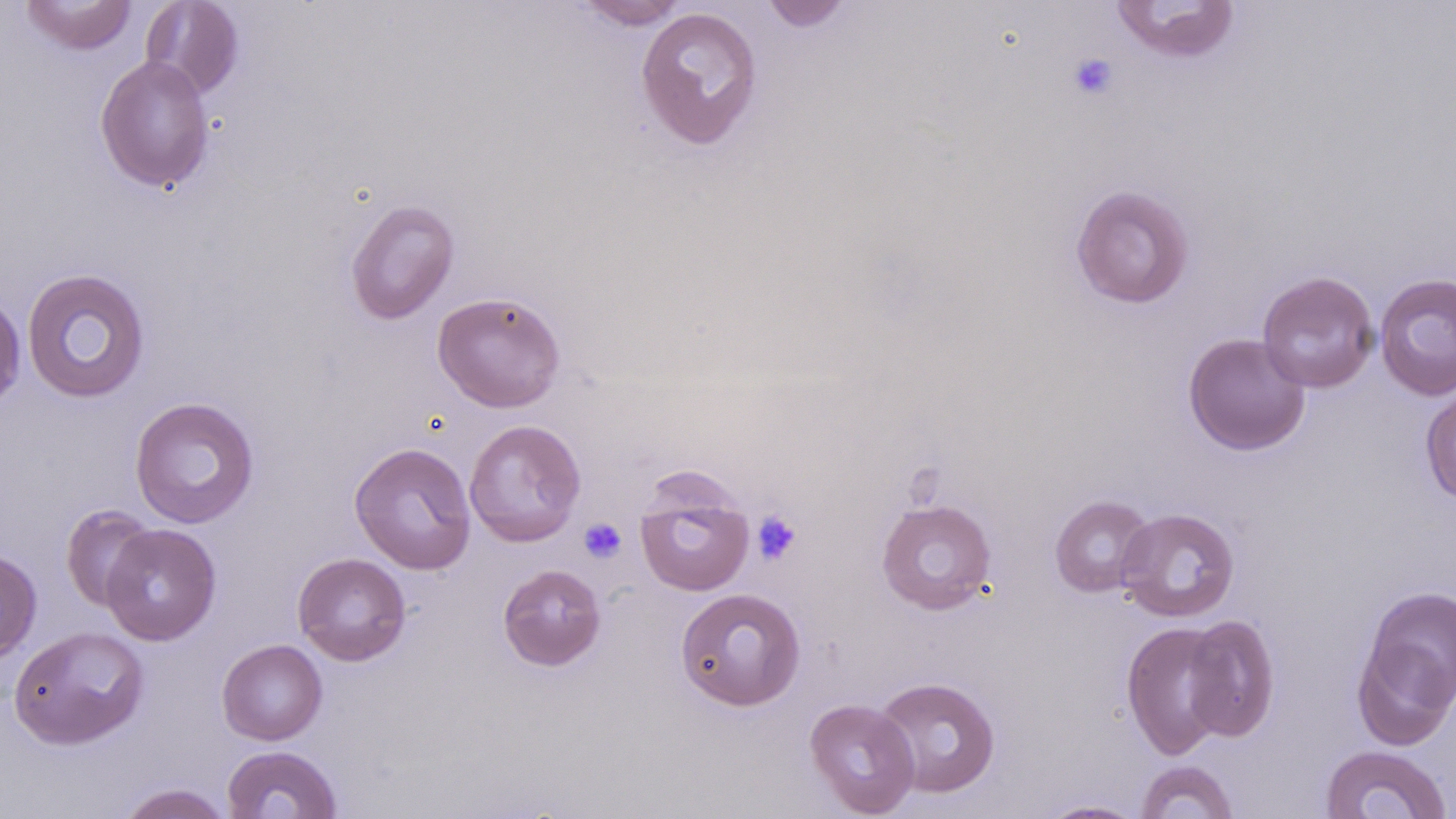
Summary:
  - Coordinate format: approximate bounding boxes as (x1,y1)-(x2,y2) corner pairs in pixels
  - Uninfected red blood cell locations: (21,0)-(137,55), (140,0)-(244,100), (1110,0)-(1241,62), (573,1)-(690,29), (759,1)-(855,32), (635,6)-(764,150), (95,55)-(215,193), (1070,184)-(1195,310), (345,197)-(460,325), (21,267)-(150,404), (1257,270)-(1380,394), (1374,273)-(1456,401), (432,291)-(566,413), (0,293)-(26,413), (1183,332)-(1311,455), (1420,386)-(1456,505), (129,396)-(260,529), (463,419)-(586,547), (349,441)-(477,575), (635,476)-(754,596), (1049,494)-(1156,598), (876,498)-(997,614), (60,504)-(158,612), (1116,507)-(1241,623), (100,523)-(222,645), (0,547)-(42,663), (292,552)-(412,666), (497,563)-(607,671), (1359,584)-(1455,715), (675,587)-(806,711), (1181,614)-(1281,742), (1120,620)-(1235,760), (9,625)-(149,749), (1351,636)-(1456,751), (216,638)-(328,745), (872,676)-(1001,798), (804,697)-(920,817), (222,744)-(343,818), (1319,744)-(1452,818), (1135,760)-(1238,819), (115,783)-(235,819), (1038,799)-(1146,818)
  - Platelet locations: (1066,52)-(1119,102), (751,510)-(802,565), (579,517)-(627,563)
  - Slide-level diagnosis: negative for blood parasites
  - Magnification: 1000x
  - Stain: May-Grünwald-Giemsa
  - Modality: light microscopy
  - Preparation: thin blood film
  - Image size: 1456×819 pixels
  - Field of view: single